Assess this cell for malaria.
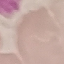
Uninfected.

preparation: thin blood smear
image_type: automatically extracted cell patch, resized to 64 × 64 pixels
capture: smartphone camera at the microscope eyepiece
stain: Giemsa